Give the position of every P. falciparum parasite, noting its life-cycle stage.
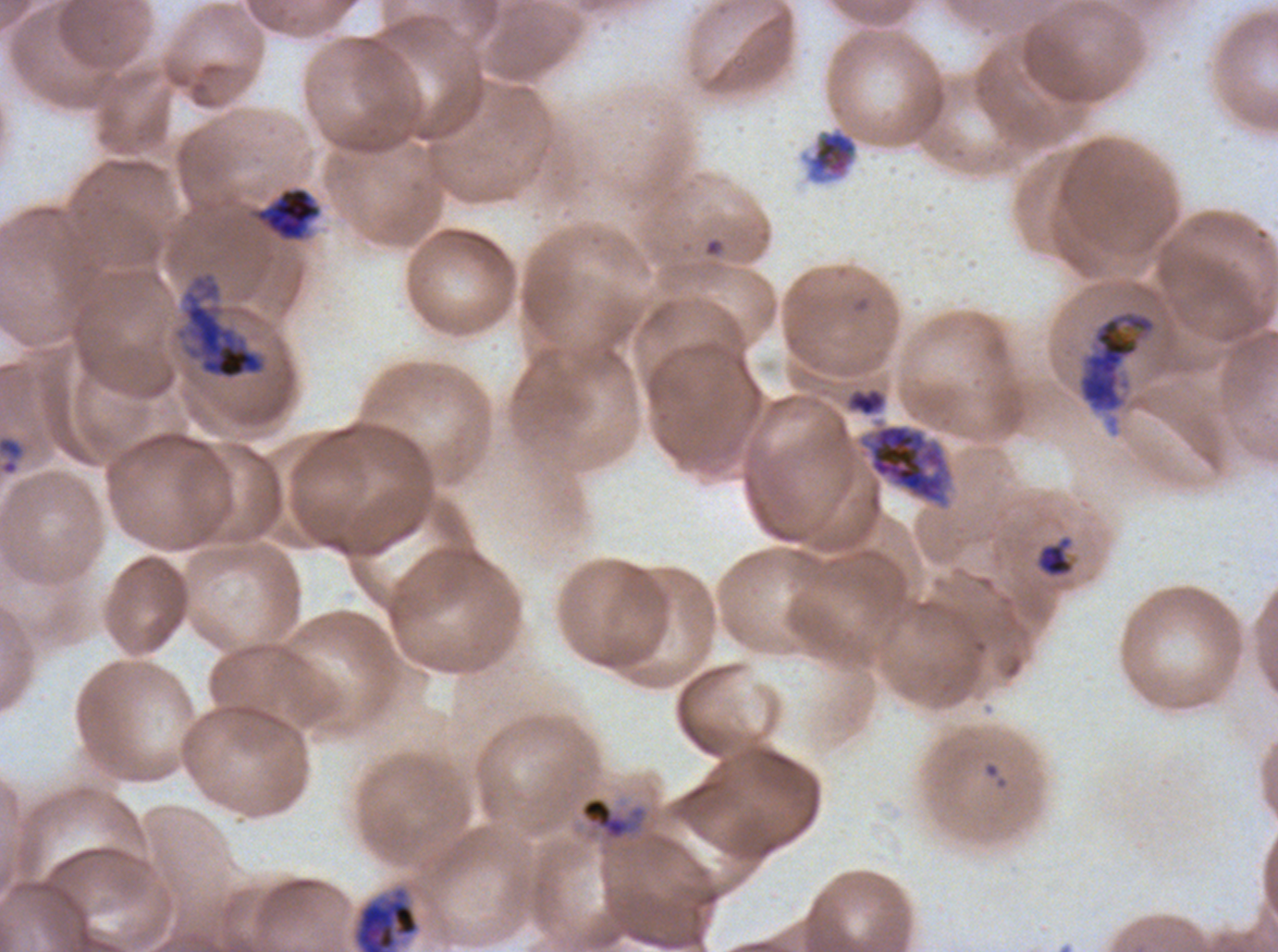
Approximate bounding boxes as [x1, y1, x2, y2] in pixels.
Rings: [0, 434, 27, 476].
Late-ring/early-trophozoite forms: [1036, 535, 1075, 578].
Early schizonts: [253, 186, 322, 242], [1075, 307, 1161, 436], [857, 422, 953, 509], [350, 884, 422, 951].
Late schizonts: [173, 270, 268, 382], [846, 386, 887, 417].
No mid trophozoites, late trophozoites, segmenters, or gametocytes observed.

Summary:
  - Debris locations: [803, 127, 859, 186], [579, 796, 646, 841]
  - Image size: 1278×952 pixels
  - Preparation: thin blood smear
  - Specimen: ex-vivo P. falciparum culture from a patient in The Gambia, grown for 24 to 48 hours
  - Life-cycle stages observed: ring, late-ring/early-trophozoite, early schizont, late schizont
  - Stain: Giemsa
  - Field of view: one sub-image of a larger composite